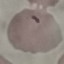

malaria status = parasitized
preparation = thin blood smear
image type = cell patch, automatically extracted from a larger field of view and resized to 64 × 64 pixels
stain = Giemsa
capture = smartphone through the microscope eyepiece